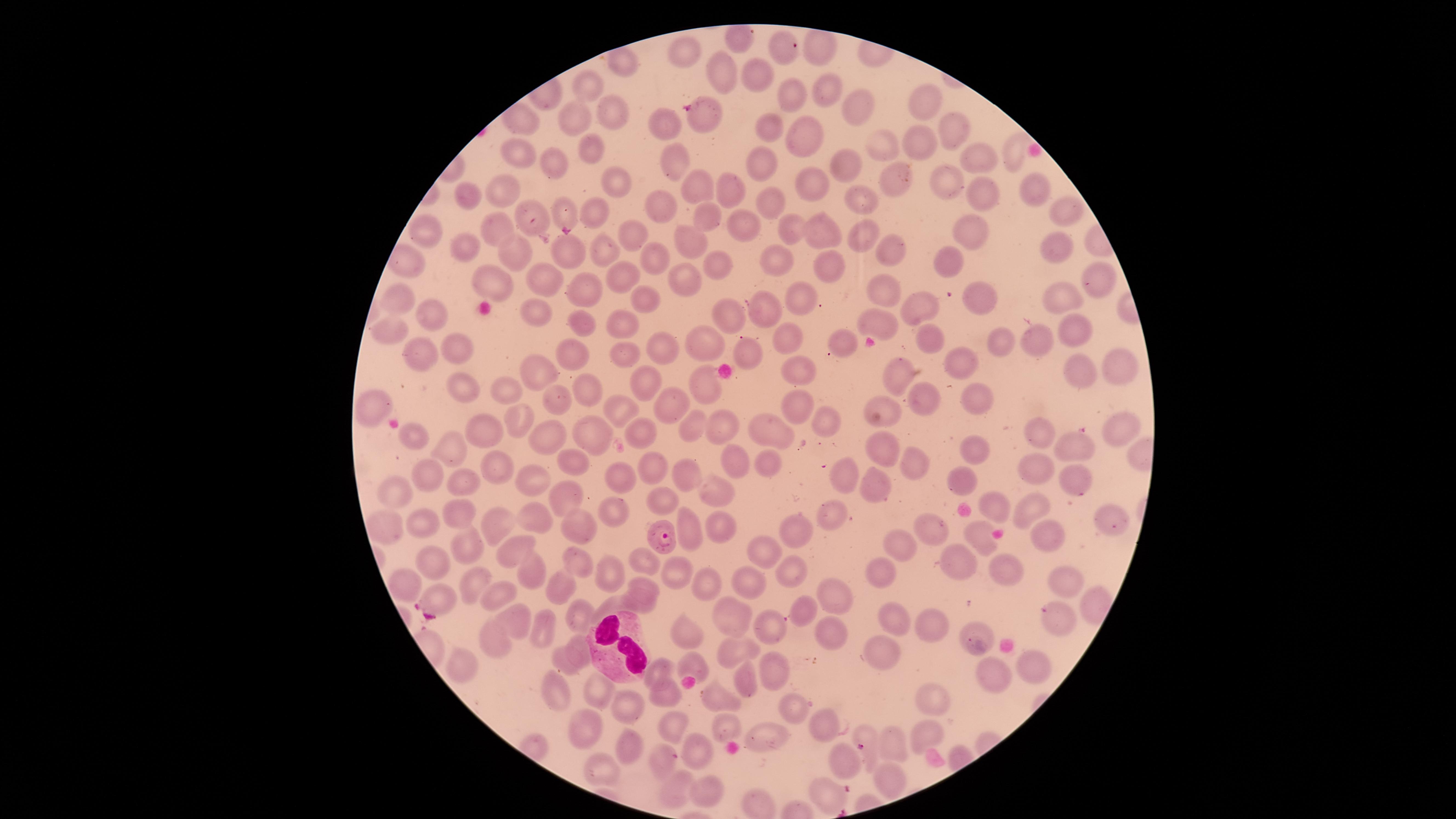
visible region = circular
WBCs = approximate marker points as (x, y) in pixels: (618, 648)
uninfected RBCs = approximate marker points as (x, y) in pixels: (738, 41), (779, 49), (686, 52), (820, 55), (622, 67), (717, 70), (755, 73), (593, 86), (826, 90), (790, 94), (925, 103), (859, 107), (614, 113), (576, 114), (705, 118), (766, 125), (669, 127), (955, 127), (805, 134), (879, 143), (915, 144), (590, 148), (523, 152), (974, 154), (672, 158), (846, 161), (763, 162), (562, 167), (616, 177), (942, 177), (893, 178), (813, 182), (726, 184), (703, 186), (1032, 189), (982, 190), (507, 192), (470, 198), (769, 200), (859, 200), (655, 202), (1066, 208), (597, 210), (567, 211), (712, 215), (537, 220), (740, 223), (493, 225), (790, 230), (821, 230), (431, 232), (636, 232), (862, 233), (977, 236), (692, 244), (467, 246), (1058, 246), (514, 250), (604, 251), (895, 251), (566, 254), (651, 260), (777, 260), (950, 263), (714, 268), (828, 268), (1097, 274), (625, 277), (680, 279), (487, 281), (544, 281), (586, 288), (875, 294), (1063, 296), (979, 297), (798, 299), (401, 300), (638, 302), (919, 303), (735, 307), (759, 310), (535, 311), (434, 318), (619, 318), (873, 319), (584, 322), (1077, 325), (388, 327), (708, 337), (932, 337), (1043, 339), (791, 340), (836, 342), (1002, 342), (460, 348), (667, 349), (747, 350), (621, 352), (574, 353), (422, 354), (966, 360), (1116, 365), (534, 367), (798, 371), (1081, 372), (900, 378), (649, 379), (703, 383), (465, 386), (506, 387), (582, 389), (977, 398), (548, 400), (926, 400), (886, 401), (670, 402), (369, 406), (799, 408), (614, 409), (516, 415), (691, 420), (825, 423), (721, 424), (481, 426), (1118, 427), (768, 431), (1041, 432), (589, 433), (644, 433), (416, 435), (551, 436), (454, 449), (972, 450), (1077, 451), (889, 452), (572, 459), (772, 462), (734, 463), (917, 463), (491, 464), (651, 468), (1038, 468), (429, 474), (683, 476), (848, 477), (617, 478), (464, 480), (535, 480), (962, 480), (1073, 483), (711, 489), (874, 490), (400, 491), (566, 496), (665, 501), (995, 507), (612, 509), (1027, 509), (462, 513), (834, 514), (1105, 517), (536, 519), (420, 521), (500, 523), (579, 527), (721, 527), (797, 527), (378, 528), (939, 528), (980, 534), (690, 535), (1047, 539), (901, 541), (468, 545), (759, 549), (512, 551), (574, 560), (960, 560), (433, 561), (646, 563), (612, 568), (1006, 568), (530, 571), (793, 573), (883, 573), (676, 575), (474, 580), (1058, 582), (642, 583), (703, 583), (746, 585), (410, 586), (563, 586), (830, 595), (439, 596), (496, 599), (613, 604), (639, 605), (730, 612), (801, 612), (579, 613), (894, 614), (515, 618), (1057, 619), (770, 626), (935, 627), (549, 629), (688, 632), (977, 633), (835, 637), (498, 640), (578, 644), (883, 646), (731, 649), (1035, 657), (467, 660), (563, 662), (767, 662), (692, 663), (663, 669), (997, 677), (744, 683), (597, 689), (555, 692), (666, 693), (930, 699), (724, 700), (634, 708), (793, 708), (726, 722), (826, 722), (585, 728), (673, 728), (865, 733), (768, 736), (922, 739), (893, 742), (634, 748), (698, 751), (842, 761), (666, 764), (603, 770), (887, 784), (677, 789), (704, 794), (828, 796)
species = Plasmodium falciparum
image size = 1456×819 pixels
parasitized RBCs = approximate marker points as (x, y) in pixels: (666, 531)
stain = Giemsa
field of view = single
presence = malaria parasites detected
capture = smartphone photograph through the microscope eyepiece
preparation = thin blood film